Classify this cell by malaria status.
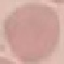
Uninfected.

{
  "capture": "smartphone through the microscope eyepiece",
  "stain": "Giemsa",
  "preparation": "thin smear",
  "image_type": "cell patch, automatically extracted from a larger field of view and resized to 64 × 64 pixels"
}